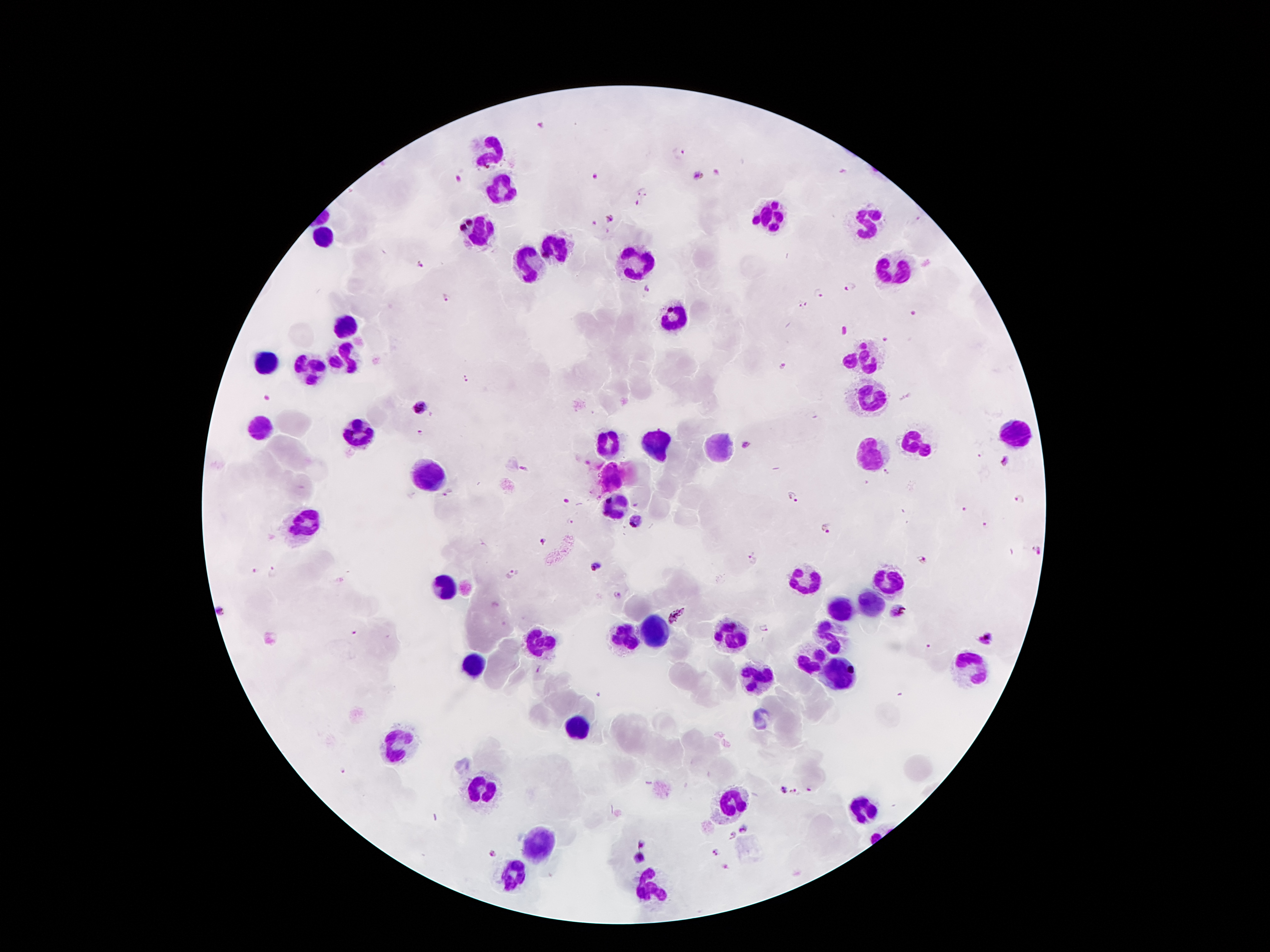
Approximate centers as {x, y} in pixels.
Summary:
  - Malaria parasite locations: {540, 125}, {679, 154}, {717, 172}, {699, 176}, {597, 177}, {457, 179}, {643, 193}, {635, 204}, {610, 218}, {919, 219}, {594, 223}, {422, 267}, {852, 285}, {647, 287}, {819, 295}, {445, 297}, {801, 305}, {886, 339}, {782, 365}, {466, 380}, {419, 407}, {420, 432}, {748, 444}, {981, 456}, {1006, 460}, {523, 468}, {888, 473}, {447, 492}, {793, 496}, {1019, 498}, {637, 503}, {965, 509}, {569, 521}, {636, 522}, {984, 523}, {826, 528}, {542, 542}, {1035, 549}, {922, 558}, {754, 559}, {595, 567}, {255, 571}, {274, 572}, {510, 574}, {618, 595}, {900, 611}, {220, 612}, {678, 617}, {764, 628}, {356, 633}, {986, 640}, {539, 670}, {344, 770}, {811, 788}, {783, 790}, {793, 792}, {746, 830}, {733, 835}, {642, 842}, {715, 853}, {492, 854}, {638, 859}, {726, 868}
  - Leukocyte locations: {488, 149}, {498, 187}, {772, 215}, {866, 219}, {482, 235}, {326, 237}, {556, 241}, {636, 257}, {528, 263}, {894, 267}, {674, 315}, {344, 325}, {342, 357}, {864, 357}, {264, 361}, {308, 367}, {868, 401}, {258, 425}, {358, 431}, {1014, 433}, {918, 439}, {604, 443}, {660, 443}, {718, 445}, {870, 453}, {430, 473}, {614, 505}, {304, 517}, {801, 581}, {892, 581}, {444, 584}, {866, 606}, {841, 609}, {730, 634}, {658, 636}, {832, 636}, {624, 638}, {540, 641}, {812, 656}, {476, 663}, {975, 664}, {837, 675}, {757, 679}, {576, 725}, {396, 743}, {483, 790}, {733, 802}, {864, 811}, {535, 840}, {515, 875}, {649, 886}
  - Magnification: 100x
  - Stain: Giemsa
  - Image size: 1270×952 pixels
  - Preparation: thick peripheral-blood smear
  - Patient malaria status: positive for Plasmodium falciparum
  - Capture: smartphone through the microscope eyepiece
  - Field of view: single